Locate every blood parasite and identify its species.
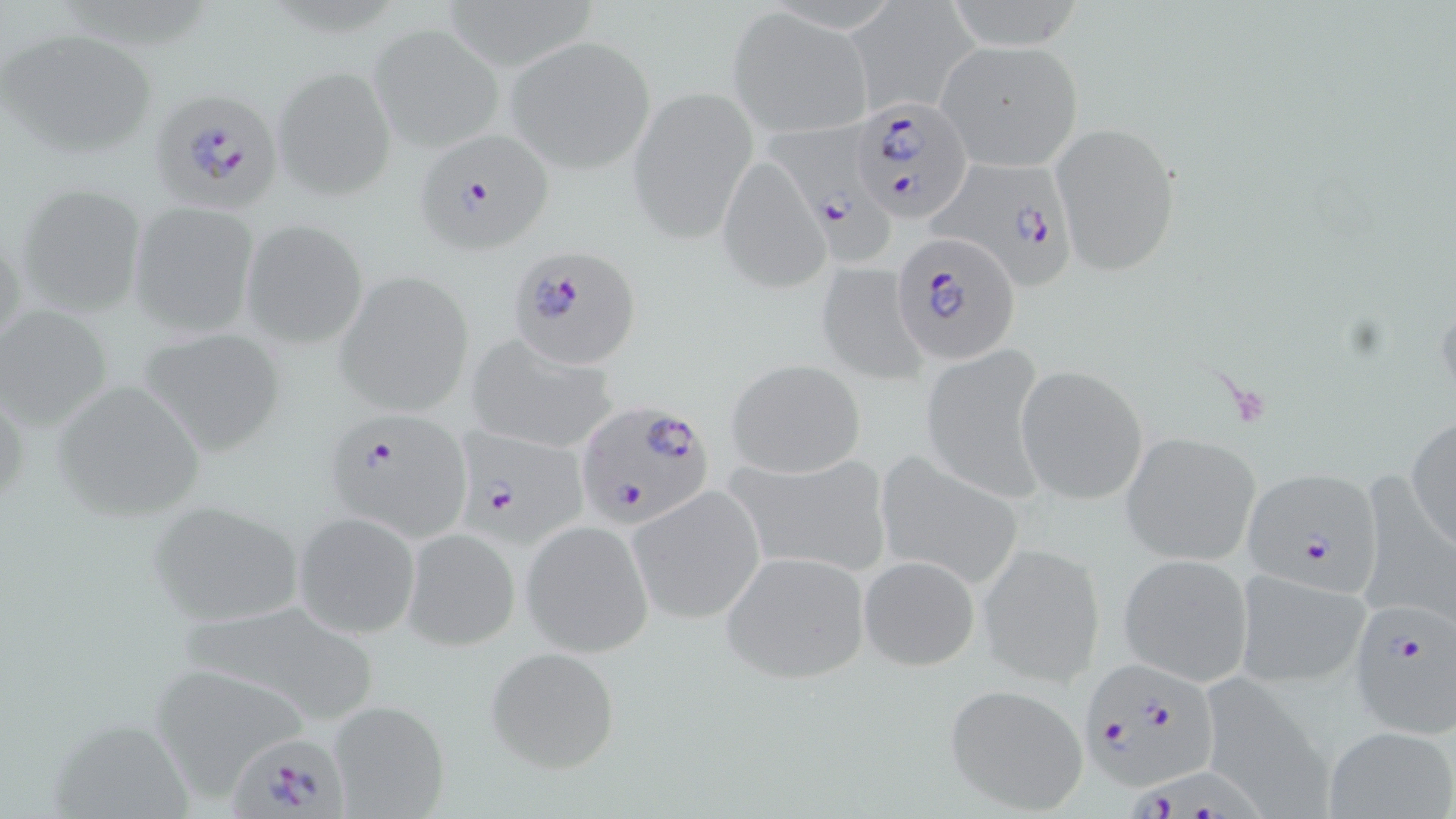

Approximate bounding boxes as [x1, y1, x2, y2] in pixels.
Plasmodium falciparum-infected red blood cells (subset): [157, 91, 284, 217], [850, 96, 972, 224], [764, 115, 896, 271], [414, 128, 558, 254], [927, 161, 1071, 281], [890, 232, 1023, 363], [507, 244, 642, 369], [576, 398, 716, 530], [321, 407, 473, 539], [451, 428, 590, 553], [1345, 601, 1455, 737], [1078, 658, 1225, 792], [228, 735, 351, 819], [1119, 757, 1280, 819].
No Plasmodium ovale, Plasmodium malariae, Plasmodium vivax, Babesia divergens, or Trypanosoma brucei observed.

slide-level diagnosis = Plasmodium falciparum
image size = 1456×819 pixels
stain = May-Grünwald-Giemsa
magnification = 1000x
modality = optical microscopy
preparation = thin blood smear
field of view = one of a larger specimen
uninfected red blood cell locations (subset) = approximate bounding boxes as [x1, y1, x2, y2] in pixels: [938, 0, 1090, 51], [847, 1, 978, 113], [727, 8, 874, 139], [369, 21, 506, 151], [0, 27, 157, 159], [504, 35, 657, 172], [936, 40, 1083, 171], [272, 65, 396, 200], [628, 86, 757, 241], [1050, 121, 1182, 276], [718, 156, 828, 293], [16, 180, 148, 318], [128, 199, 260, 337], [240, 218, 369, 351], [815, 262, 927, 385], [332, 268, 475, 418], [0, 303, 114, 430], [135, 325, 286, 458], [464, 334, 623, 456], [919, 344, 1051, 501], [725, 359, 866, 478], [1015, 364, 1150, 504], [49, 380, 207, 521], [1406, 414, 1456, 550], [1122, 432, 1260, 567], [873, 449, 1025, 591], [727, 451, 894, 582], [1365, 462, 1455, 618], [629, 487, 766, 623], [146, 499, 305, 627], [293, 511, 420, 640], [521, 519, 653, 657], [401, 526, 520, 650], [978, 541, 1107, 686], [719, 550, 871, 685], [1117, 552, 1254, 686], [858, 553, 980, 669], [1232, 566, 1373, 689], [178, 595, 383, 726], [483, 646, 621, 774], [148, 661, 309, 791], [1196, 673, 1331, 815], [942, 683, 1090, 815], [326, 698, 452, 818], [1323, 726, 1456, 819]